Name the cell type shown.
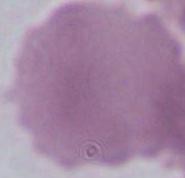

An erythrocyte.

Summary:
  - Magnification: 1000x
  - Modality: photomicrograph